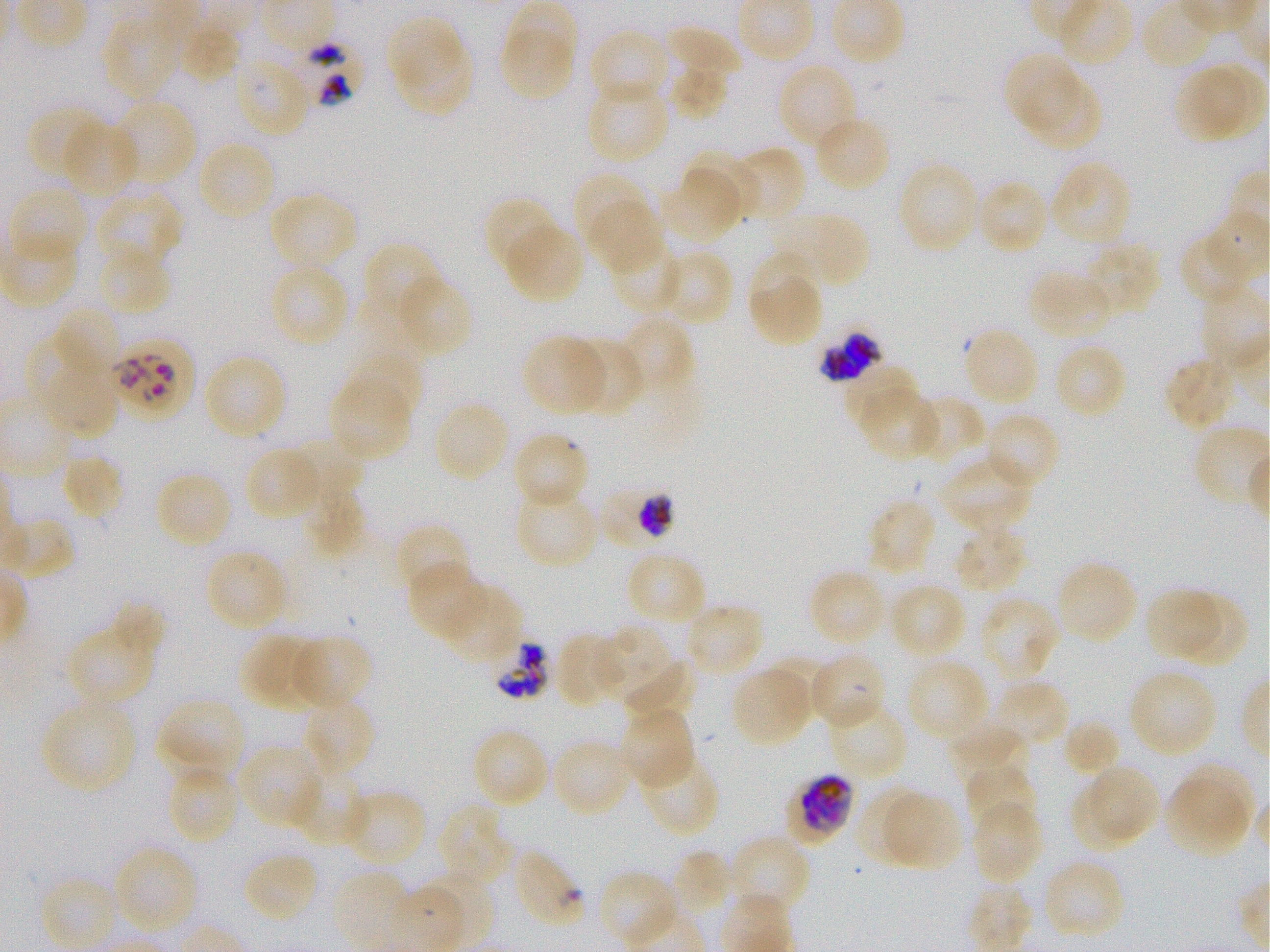
Approximate bounding boxes as {x1, y1, x2, y2} in pixels. Not every red blood cell is marked. A life-cycle stage — or a range of stages, where the recorded stages span more than one — follows each staged infected red blood cell.
Summary:
  - Locations of red blood cells of indeterminate infection status: {513, 848, 585, 929}
  - Locations of infected red blood cells: {284, 43, 364, 105}; {821, 333, 881, 384}; {107, 337, 194, 420}; {602, 487, 674, 549}; {490, 640, 548, 701}; {783, 772, 854, 847} schizont
  - Locations of uninfected red blood cells: {1140, 1, 1216, 70}, {505, 3, 576, 72}, {102, 14, 180, 101}, {387, 18, 463, 85}, {179, 20, 241, 83}, {663, 25, 742, 83}, {500, 26, 573, 101}, {587, 29, 669, 107}, {401, 41, 473, 114}, {1005, 53, 1078, 129}, {776, 61, 860, 151}, {234, 64, 307, 138}, {666, 65, 729, 122}, {1174, 68, 1246, 143}, {1030, 76, 1102, 149}, {585, 79, 670, 164}, {111, 98, 197, 186}, {27, 104, 104, 180}, {813, 115, 892, 192}, {62, 119, 138, 198}, {197, 139, 277, 223}, {732, 145, 806, 222}, {681, 150, 758, 222}, {1050, 160, 1133, 246}, {898, 161, 982, 254}, {572, 171, 647, 250}, {660, 171, 742, 243}, {977, 179, 1050, 256}, {9, 187, 88, 263}, {97, 187, 184, 270}, {276, 191, 358, 268}, {484, 197, 561, 276}, {593, 201, 663, 274}, {778, 211, 868, 287}, {505, 224, 584, 304}, {0, 233, 79, 309}, {1179, 235, 1249, 306}, {611, 240, 684, 313}, {1083, 240, 1162, 316}, {363, 243, 443, 327}, {95, 244, 172, 315}, {657, 249, 733, 327}, {751, 252, 818, 313}, {268, 263, 349, 347}, {1027, 270, 1114, 341}, {397, 275, 473, 358}, {749, 275, 822, 346}, {54, 306, 123, 379}, {620, 316, 694, 397}, {962, 326, 1040, 407}, {24, 331, 99, 412}, {521, 334, 605, 415}, {571, 338, 645, 417}, {1053, 342, 1127, 419}, {346, 346, 423, 422}, {203, 354, 288, 440}, {1164, 356, 1238, 430}, {44, 360, 118, 441}, {843, 363, 917, 430}, {329, 379, 412, 461}, {859, 389, 941, 462}, {909, 396, 985, 465}, {433, 400, 510, 483}, {984, 412, 1061, 489}, {513, 431, 590, 510}, {290, 436, 364, 503}, {243, 446, 322, 521}, {60, 453, 124, 520}, {941, 454, 1032, 533}, {154, 471, 234, 548}, {302, 485, 366, 557}, {513, 487, 600, 569}, {866, 498, 936, 576}, {6, 517, 74, 580}, {952, 523, 1029, 594}, {393, 524, 472, 599}, {204, 548, 289, 633}, {629, 556, 705, 621}, {1055, 561, 1137, 645}, {407, 565, 485, 641}, {808, 569, 887, 646}, {442, 582, 520, 665}, {888, 582, 966, 658}, {1147, 589, 1224, 663}, {1171, 592, 1248, 666}, {978, 595, 1060, 680}, {109, 603, 168, 659}, {684, 603, 764, 678}, {68, 622, 158, 705}, {593, 624, 673, 702}, {555, 631, 625, 708}, {239, 633, 319, 711}, {291, 633, 373, 712}, {810, 651, 887, 731}, {769, 656, 833, 715}, {622, 658, 695, 722}, {906, 659, 990, 742}, {730, 667, 812, 748}, {1127, 667, 1219, 757}, {992, 680, 1070, 747}, {157, 696, 244, 765}, {303, 697, 376, 776}, {39, 698, 137, 795}, {827, 699, 908, 780}, {619, 707, 696, 790}, {1061, 719, 1122, 779}, {947, 721, 1030, 785}, {470, 727, 549, 809}, {551, 738, 634, 818}, {237, 743, 324, 830}, {640, 751, 720, 836}, {1182, 762, 1256, 841}, {167, 763, 239, 845}, {964, 764, 1038, 833}, {292, 766, 366, 847}, {1092, 767, 1156, 838}, {1167, 781, 1247, 854}, {1070, 783, 1133, 851}, {857, 787, 922, 866}, {343, 789, 427, 866}, {882, 792, 961, 871}, {437, 803, 513, 886}, {972, 803, 1043, 883}, {728, 833, 812, 918}, {113, 844, 201, 934}, {672, 850, 734, 920}, {242, 851, 319, 924}, {1042, 857, 1125, 941}, {598, 870, 678, 947}, {335, 871, 412, 950}, {423, 871, 494, 944}, {38, 875, 120, 951}, {967, 882, 1033, 952}
  - Objective: 100x, oil immersion, numerical aperture 1.25
  - Stain: Giemsa
  - Image size: 1270×952 pixels
  - Culture: static in-vitro P. falciparum strain 3D7
  - Donor blood group: O+
  - Field of view: single
  - Preparation: thin blood film